Evaluate for malaria.
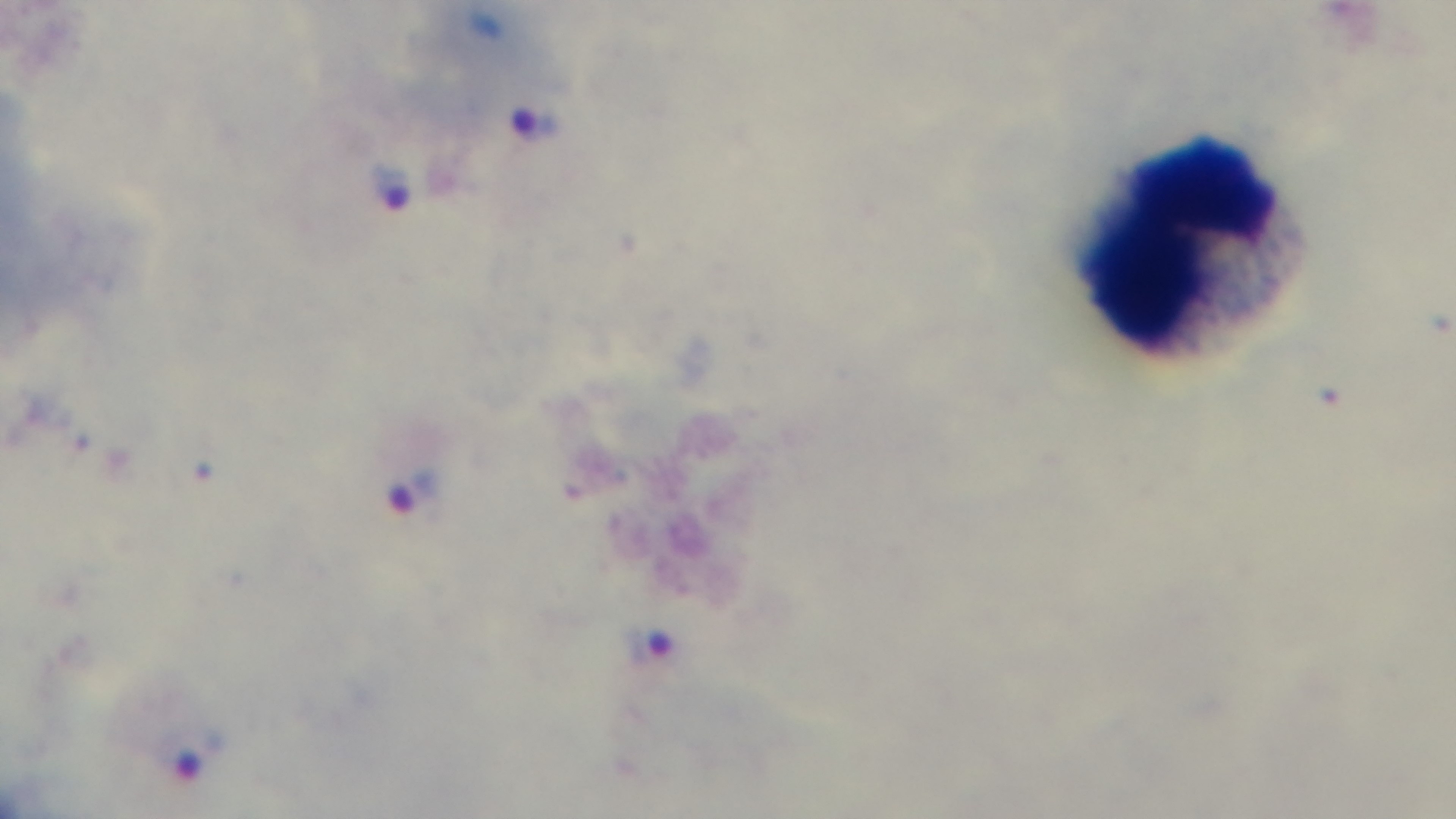

Infected.

100x oil-immersion objective. Single field of view. Preparation: thick smear. Mounted 4K digital camera. Giemsa stain. Photomicrograph.